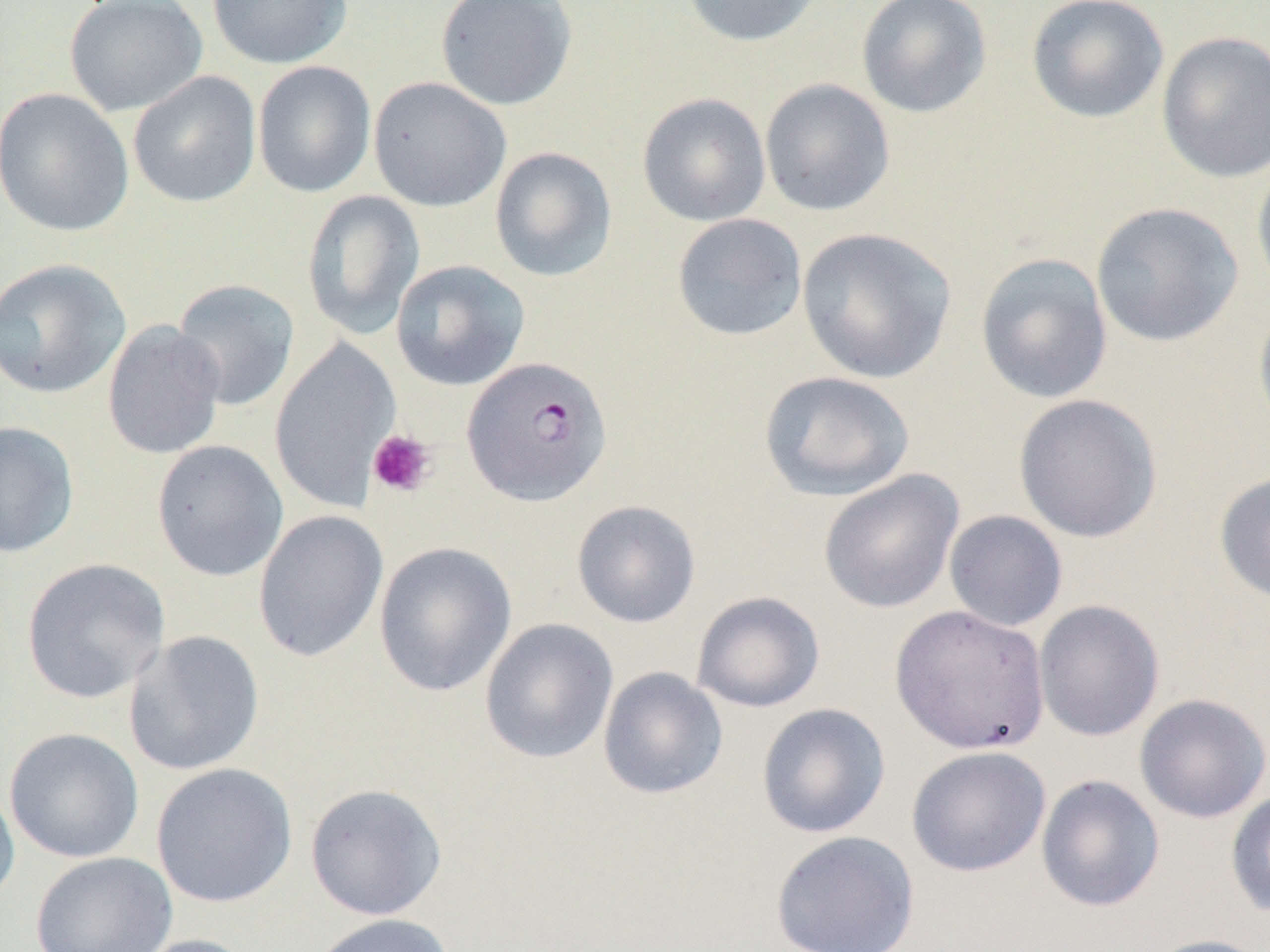
Summary:
  - Coordinate format: approximate bounding boxes as named x1/y1/x2/y2 corners in pixels
  - Platelet locations: (x1=367, y1=429, x2=436, y2=497)
  - Plasmodium falciparum-infected red blood cell locations: (x1=462, y1=356, x2=613, y2=506)
  - Uninfected red blood cell locations: (x1=64, y1=0, x2=208, y2=117), (x1=206, y1=0, x2=354, y2=70), (x1=435, y1=0, x2=577, y2=111), (x1=678, y1=0, x2=823, y2=47), (x1=856, y1=0, x2=992, y2=118), (x1=1026, y1=0, x2=1170, y2=124), (x1=1156, y1=31, x2=1270, y2=184), (x1=252, y1=60, x2=376, y2=198), (x1=127, y1=71, x2=261, y2=208), (x1=368, y1=76, x2=511, y2=212), (x1=759, y1=78, x2=896, y2=217), (x1=0, y1=87, x2=135, y2=238), (x1=637, y1=92, x2=771, y2=227), (x1=489, y1=146, x2=618, y2=282), (x1=1251, y1=159, x2=1270, y2=302), (x1=301, y1=190, x2=425, y2=340), (x1=1090, y1=202, x2=1244, y2=347), (x1=671, y1=213, x2=807, y2=341), (x1=796, y1=227, x2=956, y2=384), (x1=975, y1=252, x2=1113, y2=404), (x1=0, y1=257, x2=132, y2=399), (x1=390, y1=259, x2=530, y2=391), (x1=171, y1=278, x2=301, y2=411), (x1=1253, y1=297, x2=1270, y2=442), (x1=102, y1=320, x2=226, y2=460), (x1=269, y1=336, x2=401, y2=514), (x1=759, y1=370, x2=915, y2=502), (x1=1013, y1=393, x2=1163, y2=543), (x1=0, y1=421, x2=80, y2=558), (x1=151, y1=440, x2=288, y2=582), (x1=818, y1=469, x2=965, y2=614), (x1=1214, y1=470, x2=1270, y2=605), (x1=571, y1=499, x2=701, y2=628), (x1=253, y1=509, x2=388, y2=662), (x1=944, y1=510, x2=1068, y2=632), (x1=374, y1=541, x2=517, y2=697), (x1=21, y1=557, x2=170, y2=703), (x1=691, y1=591, x2=825, y2=713), (x1=1033, y1=599, x2=1165, y2=741), (x1=889, y1=604, x2=1051, y2=755), (x1=479, y1=618, x2=618, y2=764), (x1=124, y1=630, x2=265, y2=776), (x1=597, y1=667, x2=728, y2=800), (x1=1134, y1=693, x2=1269, y2=823), (x1=756, y1=703, x2=891, y2=838), (x1=4, y1=727, x2=145, y2=864), (x1=906, y1=745, x2=1051, y2=878), (x1=150, y1=762, x2=298, y2=909), (x1=1035, y1=774, x2=1166, y2=913), (x1=0, y1=779, x2=20, y2=910), (x1=305, y1=782, x2=448, y2=920), (x1=1225, y1=789, x2=1270, y2=918), (x1=770, y1=830, x2=921, y2=952), (x1=30, y1=851, x2=178, y2=952), (x1=305, y1=913, x2=456, y2=952), (x1=126, y1=934, x2=258, y2=952), (x1=1142, y1=934, x2=1270, y2=952)
  - Slide-level diagnosis: Plasmodium falciparum
  - Preparation: thin blood smear
  - Image size: 1270×952 pixels
  - Field of view: one of a larger specimen
  - Modality: light microscopy
  - Magnification: 1000x